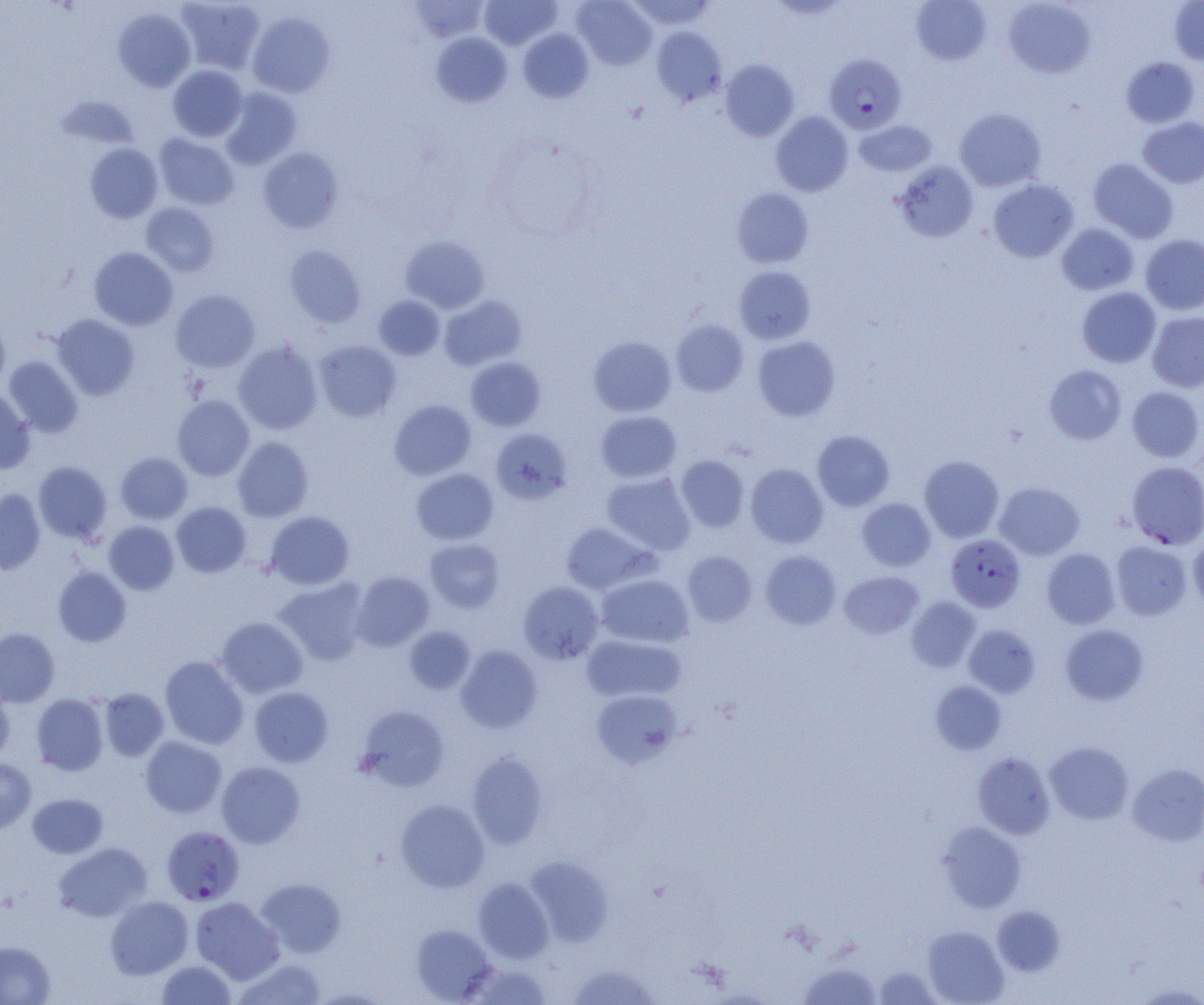
Summary:
  - Coordinate format: approximate bounding boxes as [x1, y1, x2, y2] in pixels
  - Uninfected red blood cell locations: [175, 0, 265, 74], [407, 0, 489, 43], [479, 0, 562, 49], [572, 0, 657, 69], [626, 0, 716, 30], [1003, 0, 1095, 78], [911, 1, 991, 65], [1169, 1, 1204, 65], [112, 8, 196, 92], [247, 12, 335, 98], [651, 26, 727, 106], [518, 30, 594, 102], [431, 32, 512, 107], [1121, 57, 1200, 127], [719, 59, 799, 142], [168, 65, 247, 141], [220, 88, 302, 169], [55, 94, 139, 150], [955, 108, 1047, 191], [770, 111, 853, 196], [1138, 117, 1204, 188], [854, 120, 937, 177], [154, 134, 239, 210], [85, 143, 162, 223], [258, 147, 344, 233], [1088, 158, 1178, 243], [894, 162, 978, 242], [988, 179, 1078, 262], [732, 188, 813, 268], [140, 203, 219, 277], [1057, 224, 1139, 295], [1140, 234, 1204, 315], [400, 235, 490, 313], [285, 245, 366, 328], [89, 247, 178, 330], [734, 266, 816, 343], [1077, 287, 1161, 368], [170, 289, 260, 372], [373, 295, 444, 360], [439, 295, 526, 370], [1147, 311, 1204, 392], [52, 314, 139, 400], [0, 318, 10, 392], [671, 320, 749, 396], [588, 335, 676, 416], [753, 336, 840, 421], [314, 339, 401, 422], [233, 341, 322, 434], [3, 356, 84, 437], [465, 357, 547, 431], [1044, 365, 1126, 445], [1127, 386, 1203, 462], [0, 387, 35, 473], [172, 395, 254, 480], [388, 399, 477, 480], [595, 410, 682, 482], [491, 428, 572, 504], [812, 430, 895, 511], [232, 436, 313, 522], [116, 452, 193, 524], [676, 455, 750, 532], [919, 455, 1004, 542], [33, 461, 112, 544], [745, 463, 828, 548], [412, 468, 498, 545], [601, 472, 696, 555], [995, 482, 1085, 560], [0, 488, 45, 574], [856, 498, 936, 571], [171, 502, 252, 577], [265, 511, 355, 590], [103, 521, 179, 595], [560, 523, 654, 593], [1188, 534, 1204, 612], [424, 538, 505, 612], [1111, 541, 1193, 620], [1041, 548, 1120, 629], [761, 550, 842, 629], [682, 551, 757, 626], [53, 566, 132, 647], [351, 571, 434, 651], [839, 571, 924, 639], [596, 573, 694, 648], [273, 578, 368, 666], [518, 581, 604, 664], [906, 596, 981, 672], [215, 616, 308, 698], [963, 624, 1040, 698], [1060, 624, 1149, 706], [404, 626, 476, 694], [0, 628, 60, 707], [581, 634, 686, 702], [456, 645, 543, 733], [160, 655, 249, 748], [930, 680, 1007, 755], [0, 683, 14, 762], [248, 686, 333, 767], [98, 688, 169, 761], [590, 689, 683, 768], [32, 693, 108, 776], [355, 706, 450, 792], [140, 736, 226, 818], [1044, 741, 1134, 824], [467, 751, 548, 849], [972, 752, 1056, 839], [0, 758, 37, 834], [216, 761, 305, 848], [1128, 762, 1204, 846], [27, 793, 108, 858], [395, 799, 490, 892], [938, 822, 1027, 912], [53, 842, 152, 922], [525, 856, 613, 946], [473, 877, 554, 963], [256, 878, 347, 957], [105, 896, 193, 979], [190, 896, 284, 983], [992, 905, 1065, 977], [410, 924, 496, 1003], [922, 926, 1009, 1004], [0, 941, 55, 1004], [233, 957, 328, 1004], [156, 960, 236, 1005], [464, 961, 553, 1004], [797, 962, 882, 1004], [566, 963, 660, 1004], [873, 965, 943, 1004], [1131, 982, 1204, 1004]
  - Plasmodium falciparum-infected red blood cell locations: [824, 54, 906, 133], [1126, 461, 1204, 549], [945, 533, 1025, 612], [162, 826, 244, 905]
  - Slide-level diagnosis: Plasmodium falciparum
  - Field of view: single
  - Preparation: thin blood film
  - Magnification: 1000x
  - Image size: 1204×1005 pixels
  - Modality: light microscopy